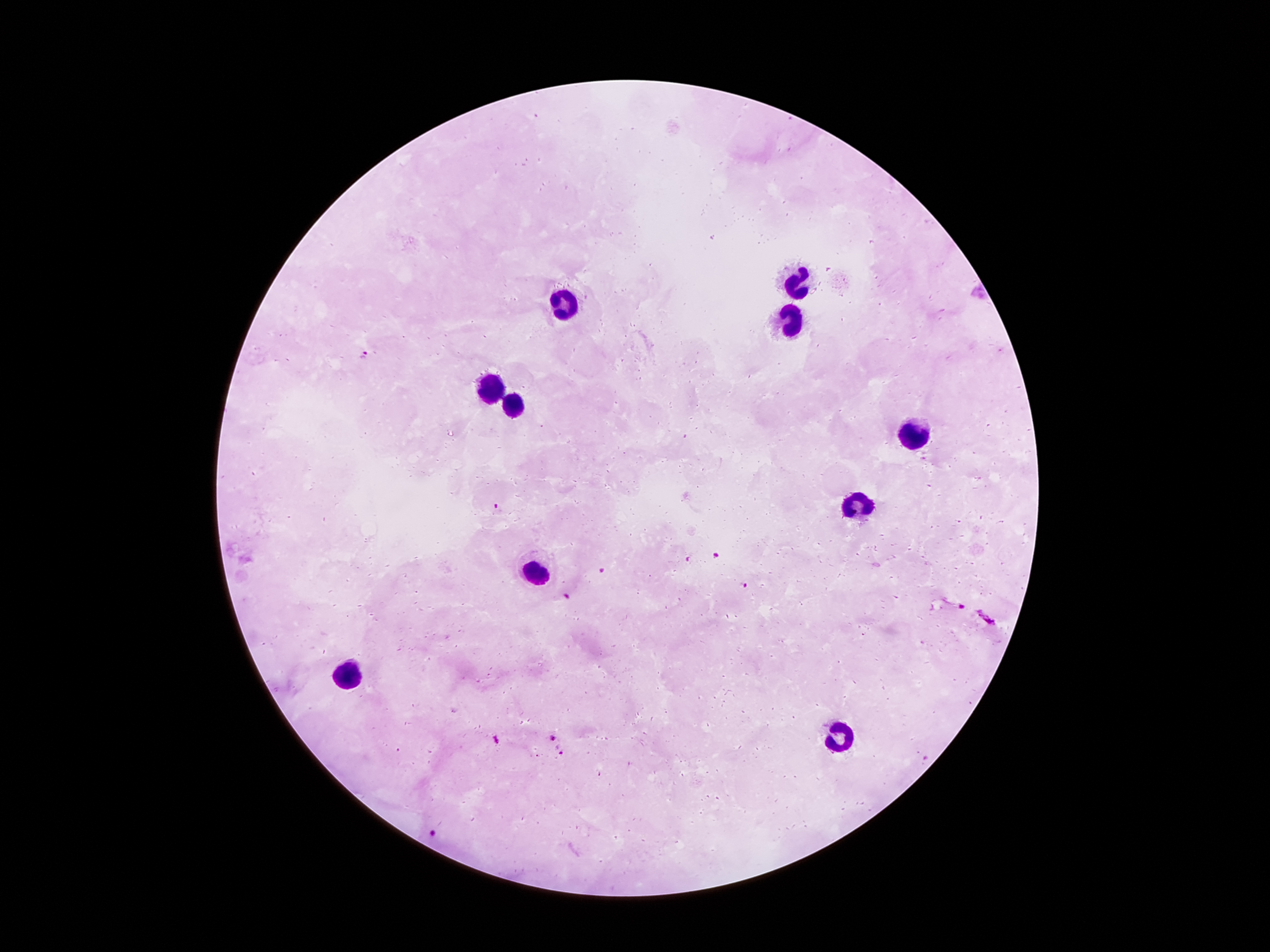

Approximate centers as (x, y) in pixels. Malaria parasite locations: (365, 354), (498, 509), (715, 555), (689, 559), (600, 570), (744, 584), (565, 596), (958, 606), (988, 618), (496, 739), (553, 740), (563, 753), (926, 758), (432, 833). Leukocyte locations: (796, 286), (566, 304), (785, 326), (491, 385), (513, 410), (920, 434), (856, 505), (537, 569), (352, 675), (838, 735). Smartphone photograph taken through the microscope eyepiece. One field from this slide. Giemsa-stained preparation. Patient malaria status: infected with Plasmodium falciparum. 100x magnification. Image is 1270×952 pixels. Thick blood film.